Give a bounding box for every leukocyte visible.
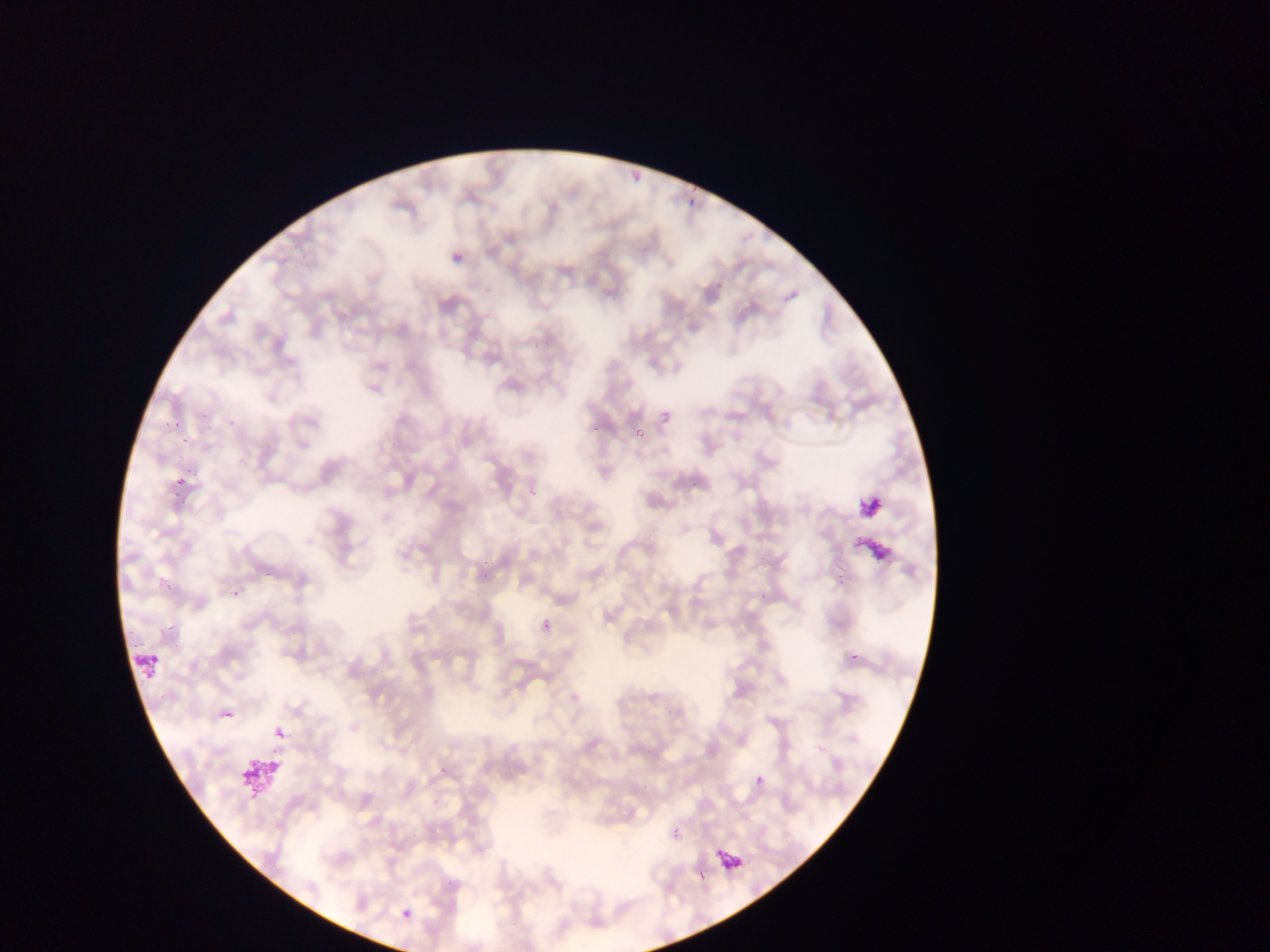
Approximate bounding boxes as (left, top, right, bottom) in pixels.
Leukocytes: (130, 650, 160, 681), (718, 845, 741, 871).

capture: mobile-phone photograph through a microscope
preparation: thin blood smear
image_size: 1270×952 pixels
field_of_view: single
country: Ghana
plasmodium_parasite_locations: 'approximate bounding boxes as (left, top, right, bottom) in pixels: (685, 196, 694, 210), (447, 250, 475, 277), (661, 411, 672, 422), (170, 417, 184, 428), (221, 418, 231, 434), (155, 420, 168, 429), (636, 428, 645, 438), (173, 448, 187, 463), (690, 480, 698, 490), (174, 483, 186, 497), (475, 558, 496, 583), (162, 576, 171, 594), (225, 586, 244, 599), (540, 618, 557, 634), (273, 726, 285, 740), (755, 775, 764, 784), (672, 829, 680, 838), (402, 909, 411, 919) | approximate (x, y) pixel centers of objects too small to bound: (184, 440)'